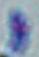

Summary:
  - Identification: Toxoplasma gondii
  - Modality: micrograph
  - Magnification: 1000x